Comment on the morphology of the erythrocytes.
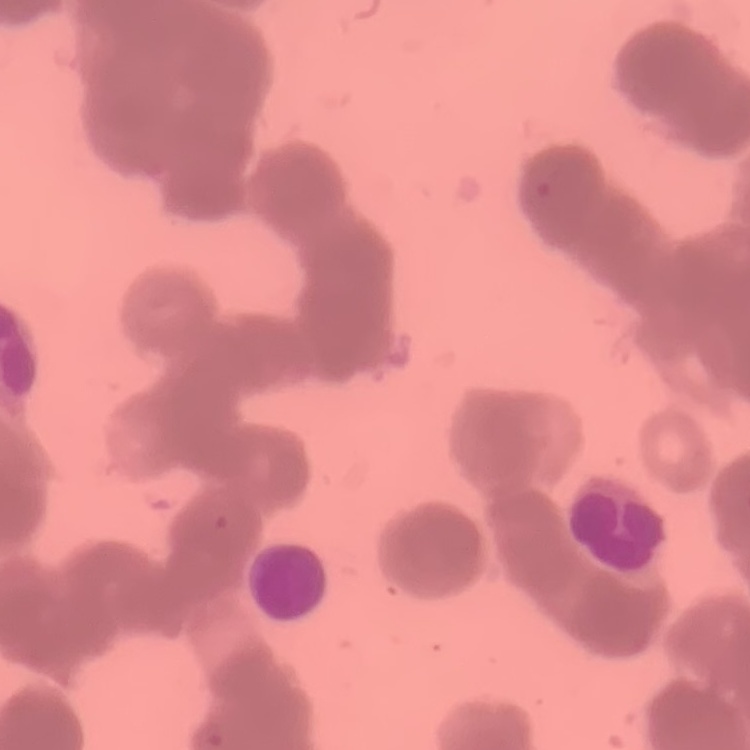
They show rouleaux formation.

One tile cut from a larger photomicrograph. Stained with either Field's or Giemsa. Thin blood film.